Give the preparation type.
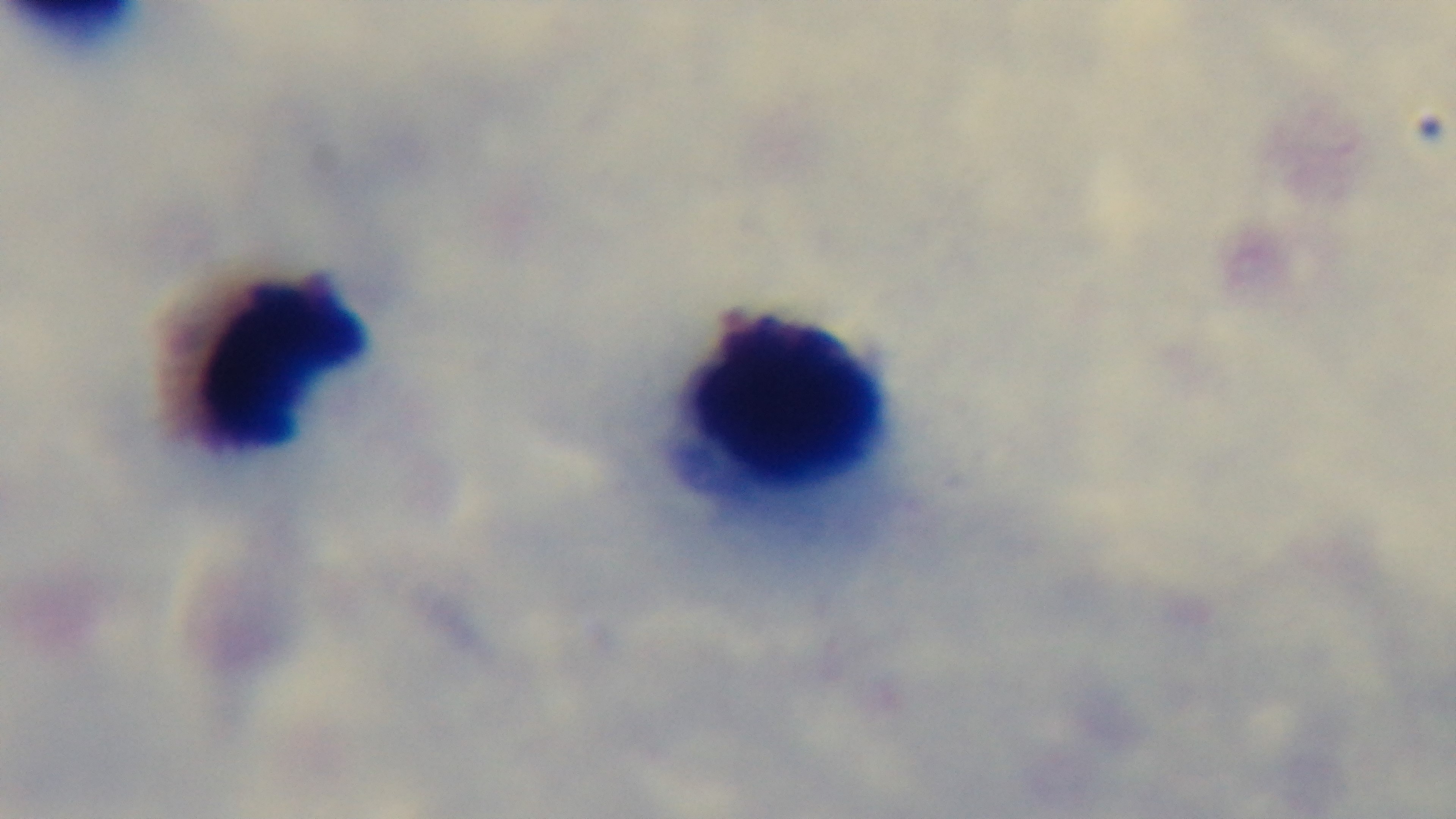

It is a thick blood film.

Malaria status: negative. Photomicrograph. Single field of view. Giemsa stain. Captured with a mounted 4K digital camera. 100x oil-immersion objective.